Assess this cell for malaria.
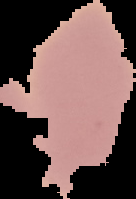

It is uninfected.

Cell region segmented out of the field of view; the surrounding area is masked to black. Image is 136×199 pixels. From a thin blood film.